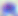
modality = photomicrograph
magnification = 400x
identification = Toxoplasma gondii